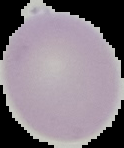

image size = 124×148 pixels
preparation = thin blood film
image type = cell region segmented out of the field of view; surrounding area masked to black
result = no malaria parasites seen